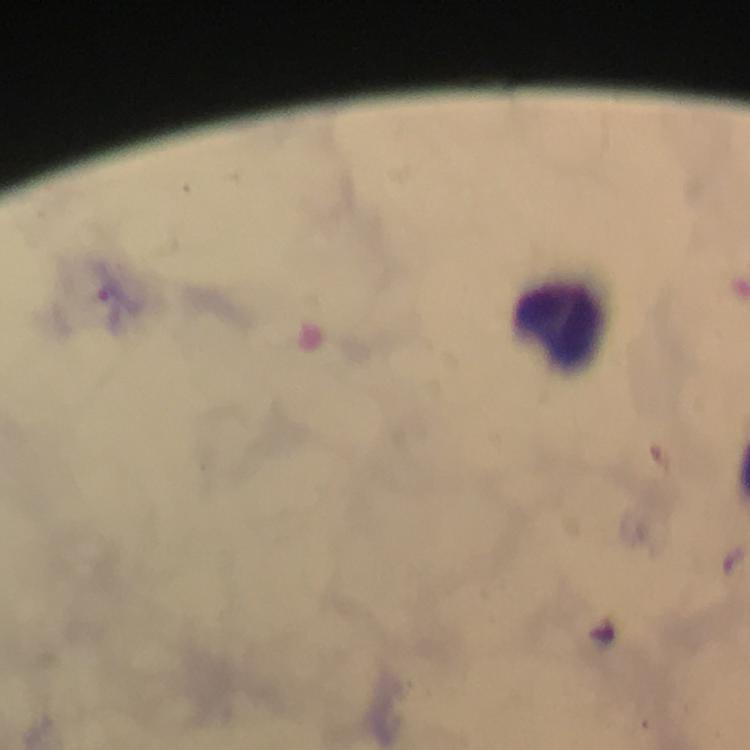
Approximate object centers, in pixels from the top-left corner. Leukocyte locations: (x=558, y=324). Malaria parasite locations: (x=115, y=296). Immersion oil applied. From a malaria diagnostic workup. At 100x magnification. Giemsa stain. Thick smear. Image is 750×750 pixels. Cropped region of a single field of view. Photographed through the microscope with a smartphone camera.